Identify the preparation type.
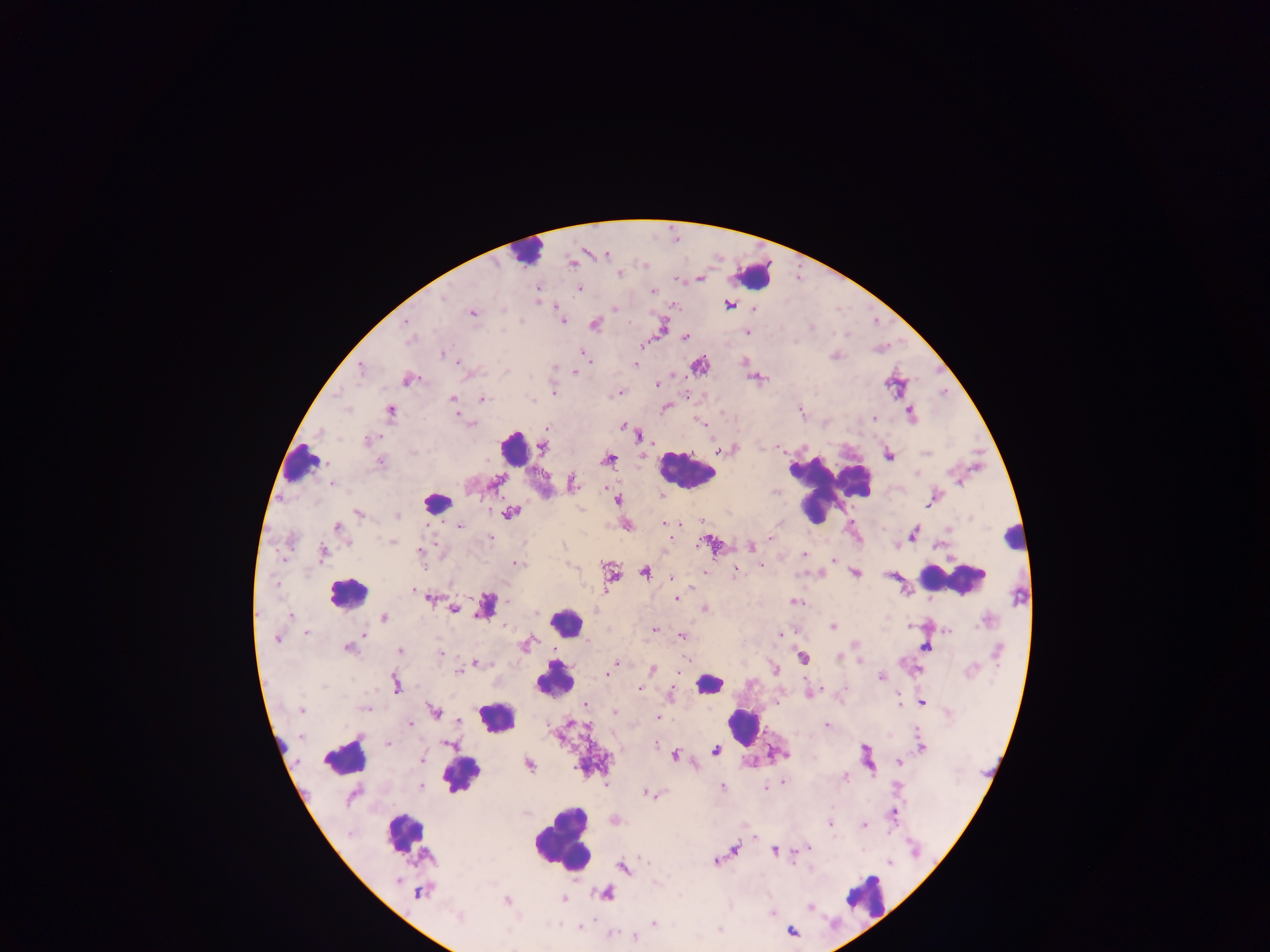
Thick blood smear.

plasmodium_parasite_locations: 'approximate centers as [x, y] in pixels: [572, 263], [619, 273], [699, 278], [536, 289], [579, 289], [653, 291], [537, 300], [729, 304], [671, 305], [615, 307], [471, 312], [406, 321], [562, 321], [594, 323], [661, 326], [747, 331], [685, 338], [409, 340], [641, 344], [442, 353], [834, 355], [585, 357], [743, 361], [635, 363], [698, 366], [361, 367], [574, 371], [757, 378], [407, 379], [656, 384], [552, 391], [619, 392], [452, 398], [481, 398], [534, 400], [665, 407], [389, 410], [800, 412], [910, 413], [456, 416], [874, 417], [701, 423], [472, 424], [623, 426], [546, 429], [638, 434], [369, 439], [543, 447], [719, 449], [723, 450], [888, 454], [641, 455], [607, 459], [379, 462], [332, 482], [495, 483], [571, 483], [660, 496], [933, 497], [617, 500], [930, 503], [358, 513], [509, 513], [397, 515], [663, 522], [459, 525], [626, 525], [337, 527], [949, 528], [913, 533], [490, 537], [770, 537], [346, 542], [393, 542], [711, 543], [751, 546], [419, 550], [321, 552], [804, 554], [834, 559], [517, 564], [760, 566], [733, 570], [644, 572], [703, 572], [610, 573], [806, 573], [855, 573], [819, 574], [891, 574], [671, 576], [429, 597], [676, 598], [794, 601], [487, 606], [703, 608], [453, 609], [290, 616], [383, 618], [910, 625], [833, 627], [654, 629], [948, 630], [306, 632], [780, 634], [682, 637], [277, 638], [525, 644], [854, 645], [925, 647], [347, 648], [400, 650], [440, 653], [838, 656], [803, 657], [859, 662], [474, 663], [615, 663], [773, 668], [611, 669], [917, 669], [653, 670], [458, 671], [680, 671], [608, 674], [881, 677], [395, 683], [638, 688], [809, 692], [671, 694], [899, 700], [921, 701], [584, 704], [365, 707], [301, 710], [434, 711], [615, 711], [657, 718], [458, 720], [410, 725], [826, 725], [387, 743], [921, 748], [716, 750], [714, 751], [674, 755], [422, 759], [899, 762], [529, 764], [844, 776], [783, 781], [421, 786], [722, 787], [764, 788], [648, 793], [654, 794], [893, 812], [614, 819], [829, 822], [863, 825], [754, 837], [808, 846], [734, 848], [774, 850], [716, 861], [622, 867], [810, 869], [420, 891], [604, 894], [563, 899], [506, 901], [810, 906], [772, 912], [654, 923], [579, 926], [719, 930], [790, 930], [610, 933], [633, 937]'
field_of_view: single
leukocyte_locations: 'approximate centers as [x, y] in pixels: [527, 250], [754, 274], [513, 447], [302, 464], [686, 471], [830, 489], [437, 502], [1013, 538], [954, 578], [346, 592], [565, 622], [553, 678], [708, 683], [496, 717], [742, 725], [344, 756], [461, 774], [404, 833], [562, 836], [864, 896]'
country: Ghana
capture: mobile-phone photograph through a microscope
image_size: 1270×952 pixels